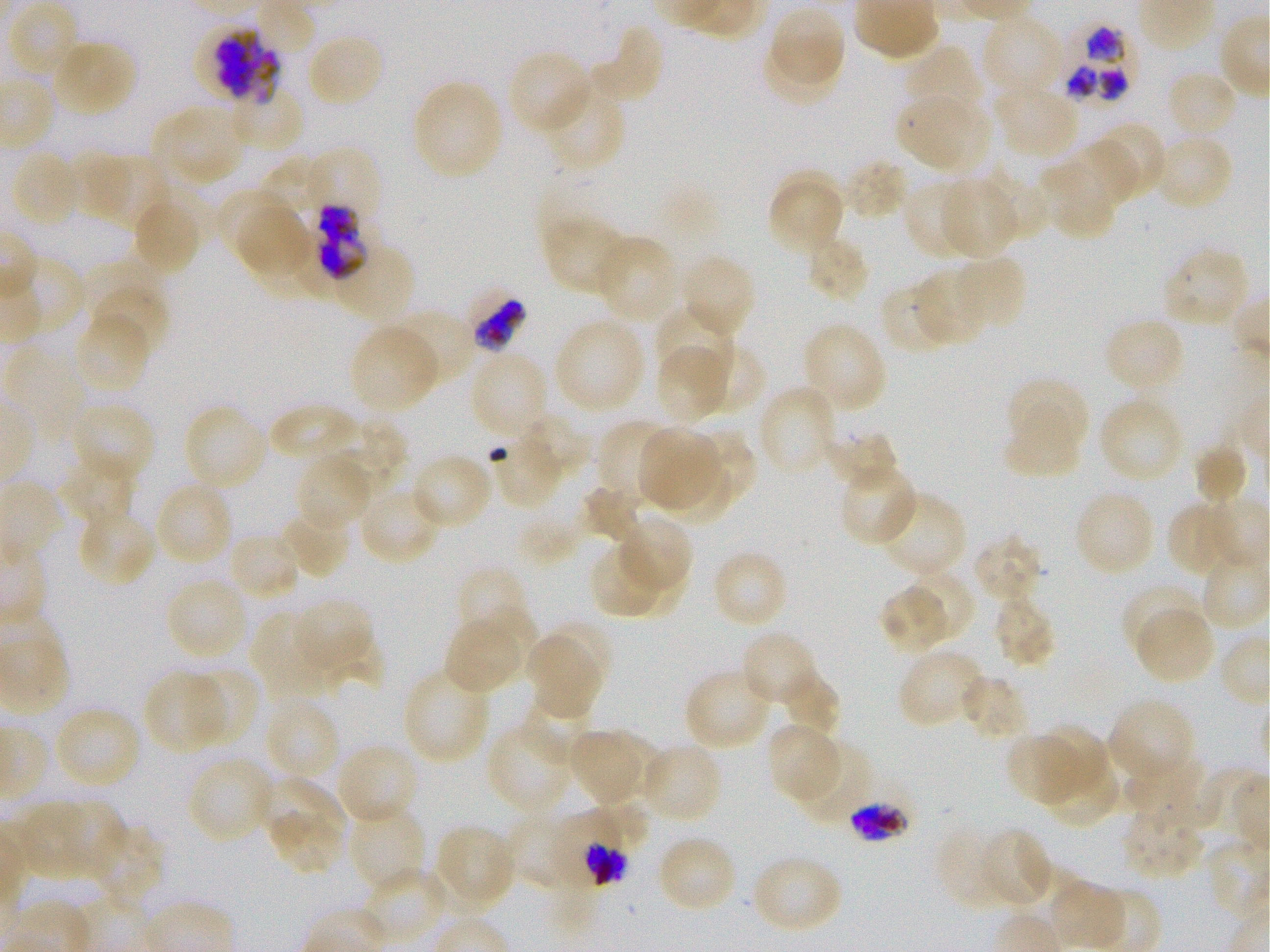
Not every red blood cell is marked. A life-cycle stage — or a range of stages, where the recorded stages span more than one — follows each staged infected red blood cell.
locations of red blood cells of indeterminate infection status = approximate bounding boxes as [x1, y1, x2, y2] in pixels: [198, 25, 281, 105], [293, 232, 354, 304], [465, 289, 525, 352], [549, 809, 629, 892]
locations of uninfected red blood cells = approximate bounding boxes as [x1, y1, x2, y2] in pixels: [255, 0, 315, 54], [8, 3, 82, 80], [770, 8, 844, 85], [981, 13, 1065, 98], [589, 24, 665, 105], [306, 32, 384, 108], [764, 39, 842, 109], [50, 40, 136, 117], [904, 47, 982, 122], [508, 49, 593, 134], [1166, 69, 1239, 140], [413, 79, 504, 179], [541, 81, 627, 173], [993, 83, 1078, 159], [228, 87, 305, 152], [896, 94, 970, 168], [930, 105, 991, 171], [156, 106, 246, 184], [1097, 125, 1164, 190], [1153, 133, 1234, 212], [1064, 139, 1139, 208], [9, 150, 82, 228], [72, 152, 139, 223], [97, 154, 171, 230], [842, 158, 910, 221], [261, 159, 325, 219], [1038, 161, 1116, 240], [982, 165, 1049, 240], [775, 170, 844, 214], [942, 179, 1018, 259], [902, 180, 977, 260], [770, 186, 840, 252], [217, 188, 293, 261], [132, 197, 201, 274], [238, 206, 315, 281], [542, 217, 629, 295], [261, 230, 317, 294], [805, 234, 871, 304], [595, 235, 678, 323], [339, 240, 421, 324], [1162, 248, 1250, 329], [680, 254, 757, 337], [12, 256, 86, 340], [953, 256, 1027, 331], [78, 260, 163, 331], [914, 267, 987, 345], [880, 282, 953, 356], [91, 286, 170, 357], [653, 304, 734, 383], [392, 309, 476, 386], [74, 313, 150, 392], [1103, 316, 1185, 393], [554, 317, 647, 412], [802, 321, 887, 412], [348, 326, 438, 412], [691, 343, 766, 416], [4, 345, 88, 442], [656, 346, 728, 423], [470, 351, 549, 436], [1006, 382, 1088, 441], [758, 385, 837, 477], [69, 402, 156, 483], [1101, 403, 1181, 480], [182, 404, 269, 492], [266, 405, 362, 470], [1002, 413, 1080, 479], [519, 415, 590, 476], [325, 418, 407, 497], [597, 419, 673, 502], [637, 427, 717, 508], [822, 428, 899, 489], [679, 429, 757, 512], [488, 432, 561, 508], [1192, 443, 1248, 506], [662, 451, 735, 524], [58, 452, 135, 529], [411, 452, 492, 529], [294, 454, 372, 532], [838, 461, 920, 546], [155, 480, 234, 566], [358, 484, 441, 565], [580, 485, 639, 542], [1075, 489, 1155, 576], [877, 491, 967, 579], [1168, 506, 1225, 573], [77, 507, 155, 586], [279, 507, 351, 579], [520, 513, 580, 565], [617, 513, 693, 595], [228, 532, 302, 600], [972, 533, 1045, 603], [592, 548, 657, 617], [711, 549, 789, 630], [625, 554, 687, 615], [456, 565, 521, 632], [905, 570, 975, 641], [165, 577, 248, 662], [1121, 582, 1200, 657], [877, 585, 952, 656], [992, 594, 1057, 670], [293, 599, 373, 669], [481, 605, 539, 680], [1135, 607, 1216, 685], [251, 612, 333, 699], [550, 620, 613, 696], [443, 621, 520, 694], [740, 631, 821, 708], [316, 633, 385, 690], [528, 636, 601, 719], [898, 649, 984, 730], [402, 666, 491, 765], [185, 667, 256, 746], [683, 669, 773, 751], [143, 671, 226, 753], [780, 674, 840, 741], [960, 674, 1029, 742], [525, 690, 594, 766], [265, 699, 341, 781], [1108, 699, 1196, 785], [61, 712, 138, 787], [487, 723, 572, 812], [765, 723, 840, 802], [1038, 724, 1108, 795], [611, 726, 669, 795], [568, 731, 637, 807], [1005, 732, 1082, 806], [795, 741, 872, 822], [640, 743, 724, 824], [336, 744, 420, 827], [1043, 754, 1120, 829], [1125, 755, 1207, 825], [187, 756, 273, 842], [1195, 766, 1266, 858], [256, 777, 348, 841], [592, 798, 651, 849], [56, 800, 126, 876], [16, 801, 95, 879], [349, 804, 425, 891], [1123, 805, 1205, 880], [268, 811, 343, 874], [506, 811, 574, 889], [435, 823, 515, 911], [93, 826, 164, 910], [936, 826, 1009, 912], [979, 828, 1052, 910], [656, 834, 737, 913], [750, 853, 843, 934], [369, 868, 450, 940], [1050, 881, 1127, 950]
locations of infected red blood cells = approximate bounding boxes as [x1, y1, x2, y2] in pixels: [1058, 24, 1138, 103]; [304, 143, 381, 219]; [312, 203, 384, 279]; [846, 798, 911, 843] early trophozoite to early schizont
stain = Giemsa
field of view = single
objective = 100x, oil immersion, numerical aperture 1.25
image size = 1270×952 pixels
preparation = thin blood film
donor blood group = O+
culture = P. falciparum strain 3D7, static, in vitro